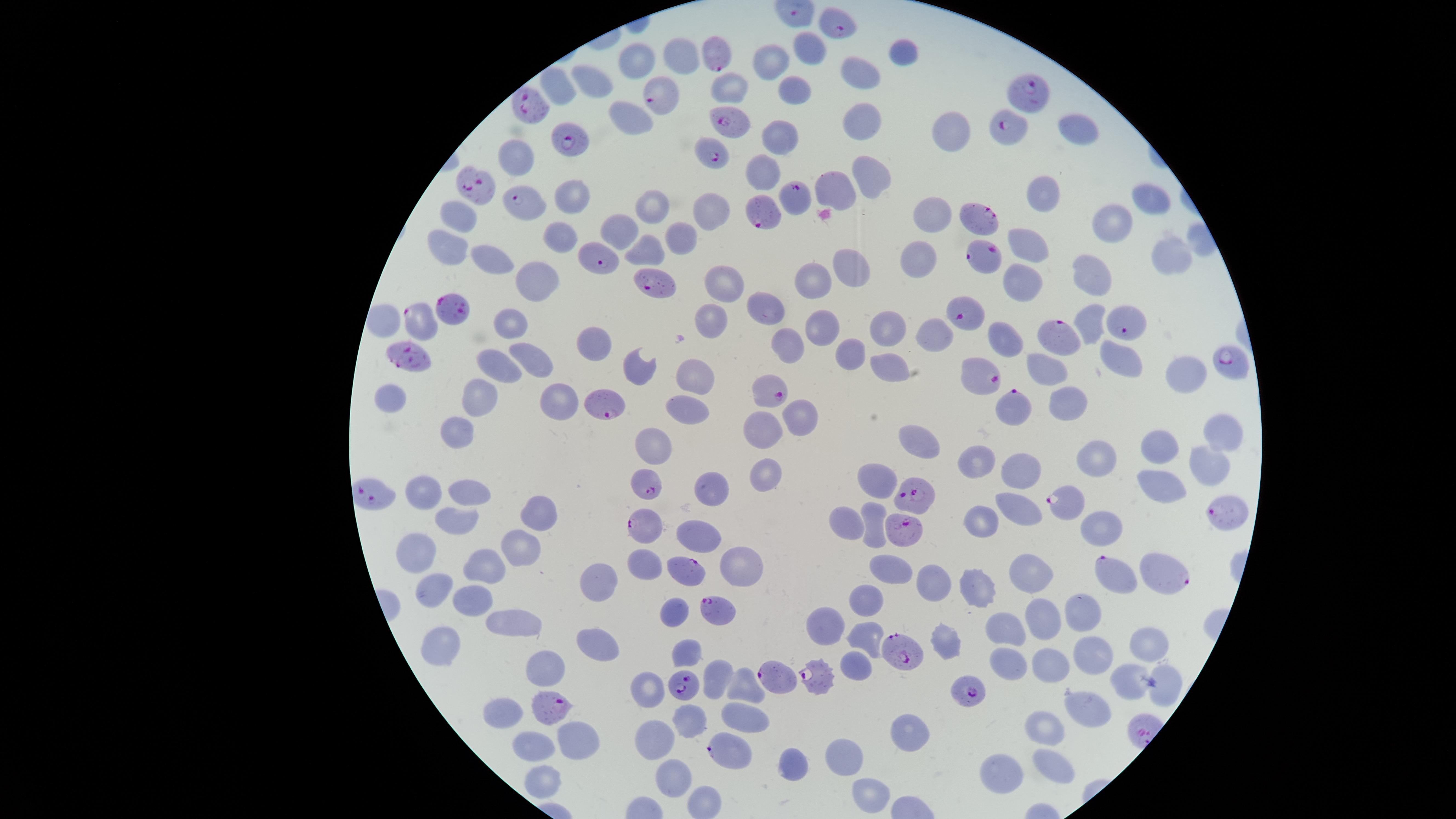
Approximate marker points, in pixels from the top-left corner. Parasitized red blood cells: (x=837, y=24), (x=713, y=53), (x=661, y=93), (x=1029, y=95), (x=528, y=103), (x=729, y=123), (x=1010, y=133), (x=571, y=140), (x=709, y=155), (x=472, y=187), (x=796, y=200), (x=526, y=203), (x=759, y=212), (x=981, y=220), (x=979, y=252), (x=600, y=255), (x=655, y=285), (x=455, y=311), (x=964, y=313), (x=418, y=318), (x=1132, y=324), (x=1054, y=335), (x=411, y=357), (x=1227, y=364), (x=981, y=374), (x=767, y=391), (x=1013, y=402), (x=607, y=405), (x=640, y=485), (x=915, y=495), (x=374, y=496), (x=1065, y=506), (x=1216, y=512), (x=642, y=526), (x=909, y=537), (x=679, y=569), (x=1164, y=574), (x=1117, y=575), (x=716, y=613), (x=904, y=655), (x=780, y=678), (x=820, y=679), (x=682, y=685), (x=972, y=694), (x=551, y=708), (x=729, y=751). Uninfected red blood cells: (x=809, y=47), (x=903, y=49), (x=770, y=53), (x=681, y=56), (x=633, y=63), (x=859, y=71), (x=593, y=83), (x=561, y=84), (x=736, y=84), (x=792, y=93), (x=635, y=116), (x=858, y=124), (x=949, y=128), (x=1078, y=128), (x=773, y=142), (x=514, y=160), (x=765, y=172), (x=868, y=175), (x=836, y=189), (x=1046, y=194), (x=1146, y=198), (x=572, y=200), (x=654, y=203), (x=711, y=210), (x=461, y=215), (x=928, y=215), (x=1115, y=224), (x=621, y=228), (x=685, y=235), (x=556, y=241), (x=1025, y=242), (x=450, y=246), (x=648, y=249), (x=491, y=258), (x=853, y=259), (x=1166, y=259), (x=913, y=262), (x=1094, y=275), (x=722, y=282), (x=817, y=282), (x=1022, y=282), (x=534, y=285), (x=768, y=304), (x=711, y=311), (x=818, y=316), (x=1091, y=319), (x=513, y=320), (x=890, y=333), (x=928, y=334), (x=1002, y=342), (x=789, y=345), (x=587, y=346), (x=846, y=356), (x=1116, y=359), (x=531, y=360), (x=644, y=361), (x=504, y=365), (x=1053, y=366), (x=890, y=369), (x=1183, y=373), (x=691, y=380), (x=387, y=393), (x=477, y=398), (x=1067, y=402), (x=556, y=403), (x=684, y=410), (x=798, y=420), (x=1221, y=431), (x=759, y=435), (x=449, y=439), (x=919, y=445), (x=650, y=447), (x=1151, y=447), (x=1099, y=455), (x=975, y=459), (x=1210, y=459), (x=1020, y=467), (x=767, y=472), (x=876, y=482), (x=1157, y=482), (x=471, y=487), (x=715, y=489), (x=426, y=490), (x=546, y=513), (x=1024, y=513), (x=448, y=519), (x=987, y=523), (x=842, y=526), (x=871, y=527), (x=1105, y=528), (x=697, y=530), (x=523, y=542), (x=419, y=557), (x=645, y=563), (x=489, y=564), (x=735, y=567), (x=892, y=571), (x=1037, y=576), (x=978, y=583), (x=597, y=584), (x=933, y=584), (x=438, y=594), (x=475, y=597), (x=870, y=600), (x=674, y=608), (x=1084, y=611), (x=1049, y=616), (x=827, y=624), (x=516, y=625), (x=1008, y=627), (x=594, y=638), (x=865, y=639), (x=943, y=641), (x=440, y=642), (x=1152, y=645), (x=684, y=652), (x=1092, y=656), (x=1005, y=657), (x=1057, y=663), (x=854, y=667), (x=545, y=669), (x=715, y=676), (x=1163, y=685), (x=738, y=690), (x=649, y=691), (x=1086, y=707), (x=746, y=715), (x=501, y=716), (x=690, y=726), (x=1048, y=729), (x=905, y=733), (x=582, y=738), (x=654, y=741), (x=538, y=748), (x=849, y=748), (x=797, y=766), (x=1050, y=768), (x=1000, y=778), (x=669, y=780), (x=538, y=784), (x=871, y=796). Image is 1456×819 pixels. Giemsa-stained preparation. Thin smear of blood. One field of view of the specimen. Presence: malaria parasites seen. The visible region is circular. Species: Plasmodium falciparum. Smartphone photograph through the microscope eyepiece.